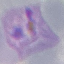

Result: malaria parasites detected. Automatically extracted cell patch, resized to 64 × 64 pixels. Acquired by smartphone through the microscope eyepiece. Thin blood smear. Giemsa-stained preparation.